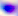
modality: micrograph
magnification: 400x
identification: Toxoplasma gondii